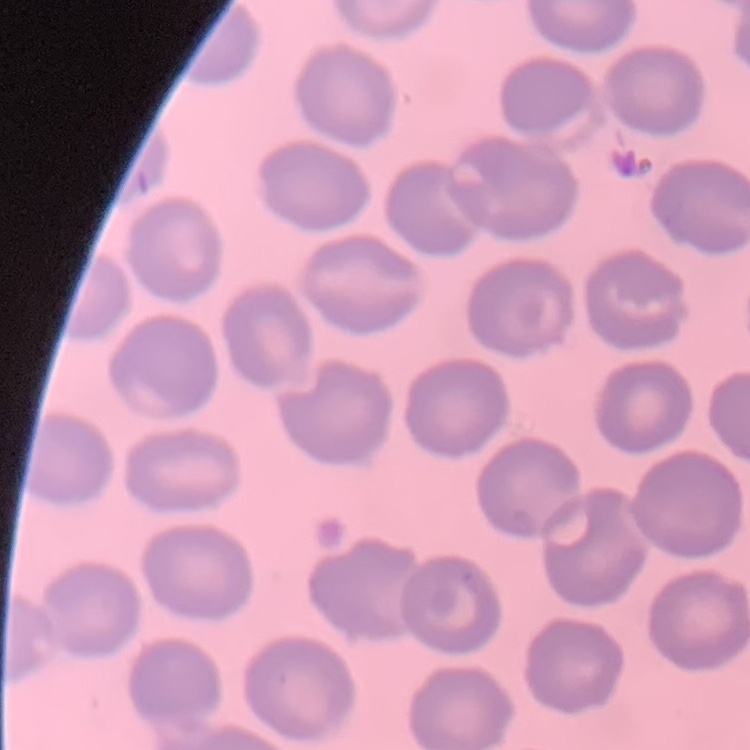 The erythrocytes exhibit no rouleaux formation. Field's or Giemsa stain. Square crop of a larger photomicrograph. Thin blood film.